Point out each leukocyte.
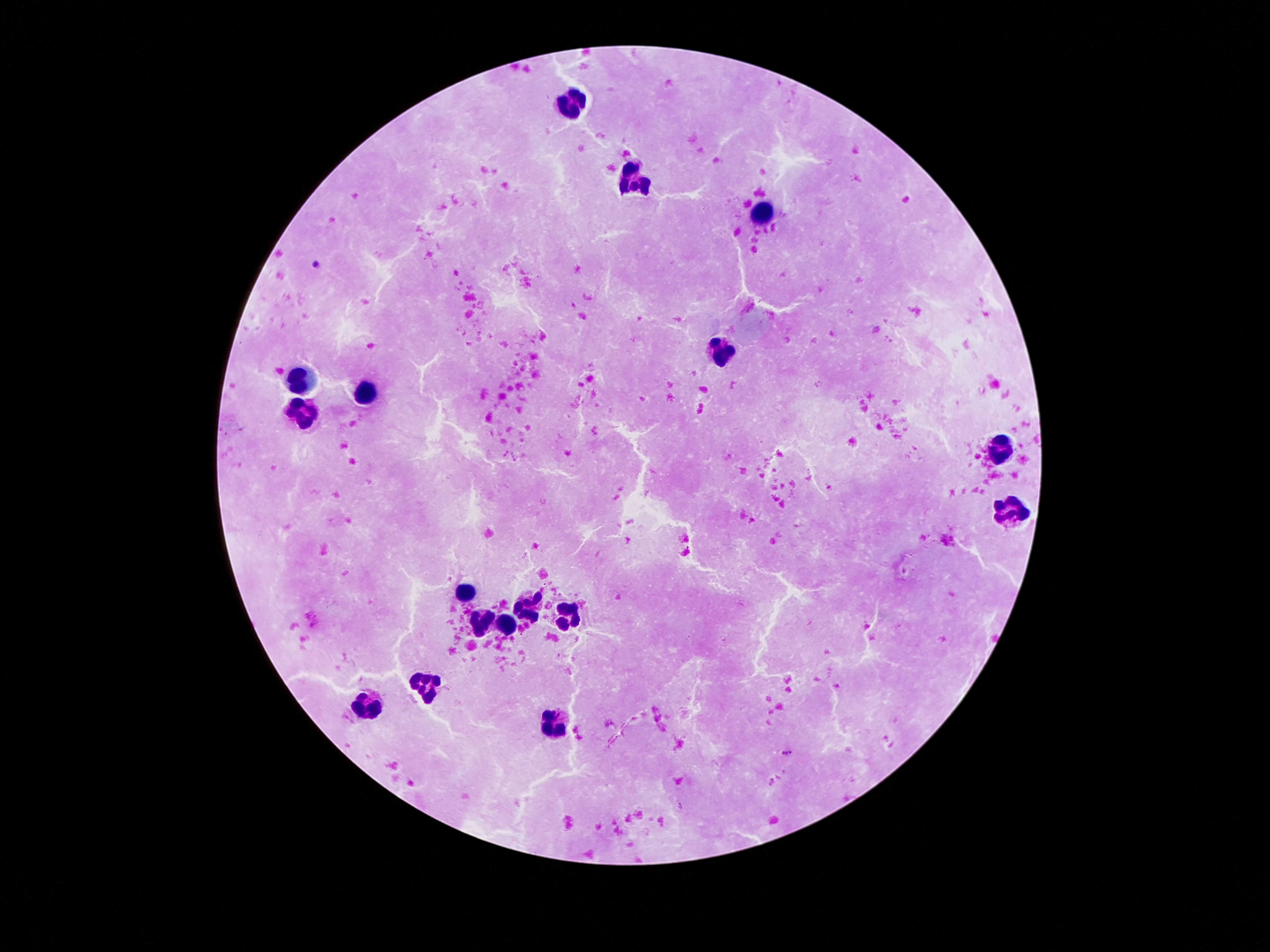

Approximate object centers, in pixels from the top-left corner.
Leukocytes: (x=573, y=104), (x=634, y=181), (x=763, y=215), (x=722, y=353), (x=300, y=378), (x=369, y=388), (x=302, y=411), (x=996, y=451), (x=1008, y=511), (x=464, y=589), (x=528, y=606), (x=569, y=615), (x=479, y=624), (x=509, y=626), (x=425, y=684), (x=367, y=705), (x=552, y=723).

{
  "magnification": "100x",
  "patient_malaria_status": "negative",
  "capture": "smartphone camera through the microscope eyepiece",
  "stain": "Giemsa",
  "preparation": "thick peripheral-blood smear",
  "image_size": "1270×952 pixels",
  "field_of_view": "single"
}